Classify this cell by malaria status.
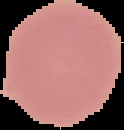

Uninfected.

The area outside the segmented cell region is set to black. Image is 124×130 pixels. From a thin blood film.